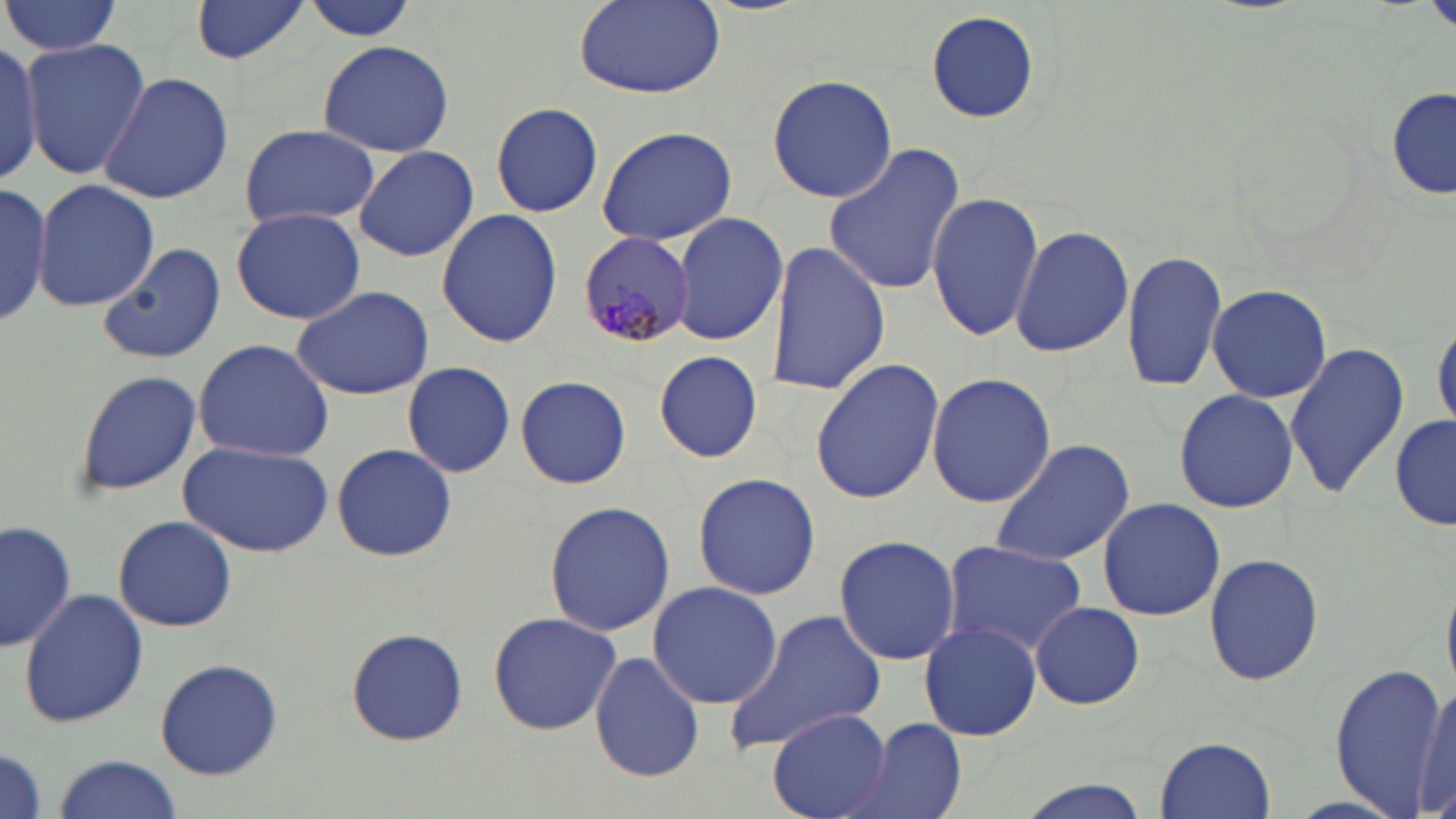
Approximate bounding boxes as named x1/y1/x2/y2 corners in pixels. Plasmodium malariae-infected red blood cell locations: (x1=577, y1=231, x2=693, y2=348). Uninfected red blood cell locations: (x1=2, y1=0, x2=123, y2=58), (x1=190, y1=0, x2=308, y2=64), (x1=573, y1=0, x2=726, y2=100), (x1=298, y1=1, x2=419, y2=43), (x1=1424, y1=1, x2=1456, y2=35), (x1=927, y1=11, x2=1040, y2=125), (x1=21, y1=39, x2=150, y2=180), (x1=316, y1=39, x2=455, y2=159), (x1=0, y1=41, x2=43, y2=186), (x1=99, y1=71, x2=232, y2=206), (x1=768, y1=73, x2=897, y2=204), (x1=1387, y1=88, x2=1454, y2=203), (x1=489, y1=102, x2=605, y2=219), (x1=239, y1=124, x2=381, y2=229), (x1=595, y1=125, x2=737, y2=245), (x1=352, y1=144, x2=480, y2=262), (x1=823, y1=144, x2=965, y2=297), (x1=34, y1=178, x2=158, y2=314), (x1=0, y1=185, x2=57, y2=323), (x1=926, y1=191, x2=1044, y2=343), (x1=230, y1=208, x2=366, y2=324), (x1=436, y1=208, x2=562, y2=347), (x1=671, y1=211, x2=789, y2=345), (x1=1010, y1=225, x2=1135, y2=359), (x1=765, y1=240, x2=889, y2=396), (x1=99, y1=243, x2=226, y2=365), (x1=1121, y1=248, x2=1230, y2=394), (x1=1205, y1=282, x2=1333, y2=405), (x1=288, y1=284, x2=438, y2=401), (x1=1433, y1=321, x2=1455, y2=433), (x1=191, y1=338, x2=335, y2=462), (x1=1285, y1=340, x2=1410, y2=497), (x1=652, y1=352, x2=765, y2=460), (x1=809, y1=359, x2=945, y2=507), (x1=402, y1=361, x2=517, y2=475), (x1=73, y1=368, x2=199, y2=497), (x1=925, y1=373, x2=1057, y2=508), (x1=513, y1=375, x2=632, y2=491), (x1=1173, y1=388, x2=1299, y2=514), (x1=1391, y1=416, x2=1454, y2=532), (x1=987, y1=439, x2=1135, y2=567), (x1=179, y1=441, x2=333, y2=558), (x1=329, y1=442, x2=459, y2=564), (x1=693, y1=471, x2=819, y2=600), (x1=1096, y1=497, x2=1225, y2=623), (x1=543, y1=498, x2=676, y2=636), (x1=112, y1=515, x2=237, y2=633), (x1=1, y1=517, x2=77, y2=654), (x1=833, y1=534, x2=961, y2=666), (x1=939, y1=540, x2=1090, y2=658), (x1=1203, y1=553, x2=1326, y2=687), (x1=648, y1=581, x2=782, y2=708), (x1=18, y1=589, x2=149, y2=727), (x1=1029, y1=602, x2=1144, y2=710), (x1=722, y1=608, x2=886, y2=758), (x1=486, y1=611, x2=623, y2=736), (x1=919, y1=621, x2=1041, y2=741), (x1=346, y1=628, x2=468, y2=746), (x1=589, y1=649, x2=703, y2=783), (x1=154, y1=657, x2=283, y2=781), (x1=1329, y1=662, x2=1452, y2=816), (x1=1413, y1=679, x2=1456, y2=816), (x1=770, y1=709, x2=889, y2=818), (x1=857, y1=718, x2=967, y2=819), (x1=1155, y1=736, x2=1276, y2=818), (x1=0, y1=743, x2=48, y2=819), (x1=55, y1=754, x2=182, y2=817), (x1=1011, y1=781, x2=1151, y2=819). Slide-level diagnosis: Plasmodium malariae. Image is 1456×819 pixels. Thin blood film. Single field of view. Captured at 1000x magnification. Optical microscopy. May-Grünwald-Giemsa stain.